State which cell type is depicted.
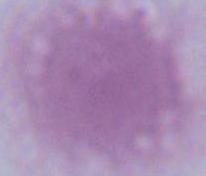
An erythrocyte.

1000x magnification. Micrograph.